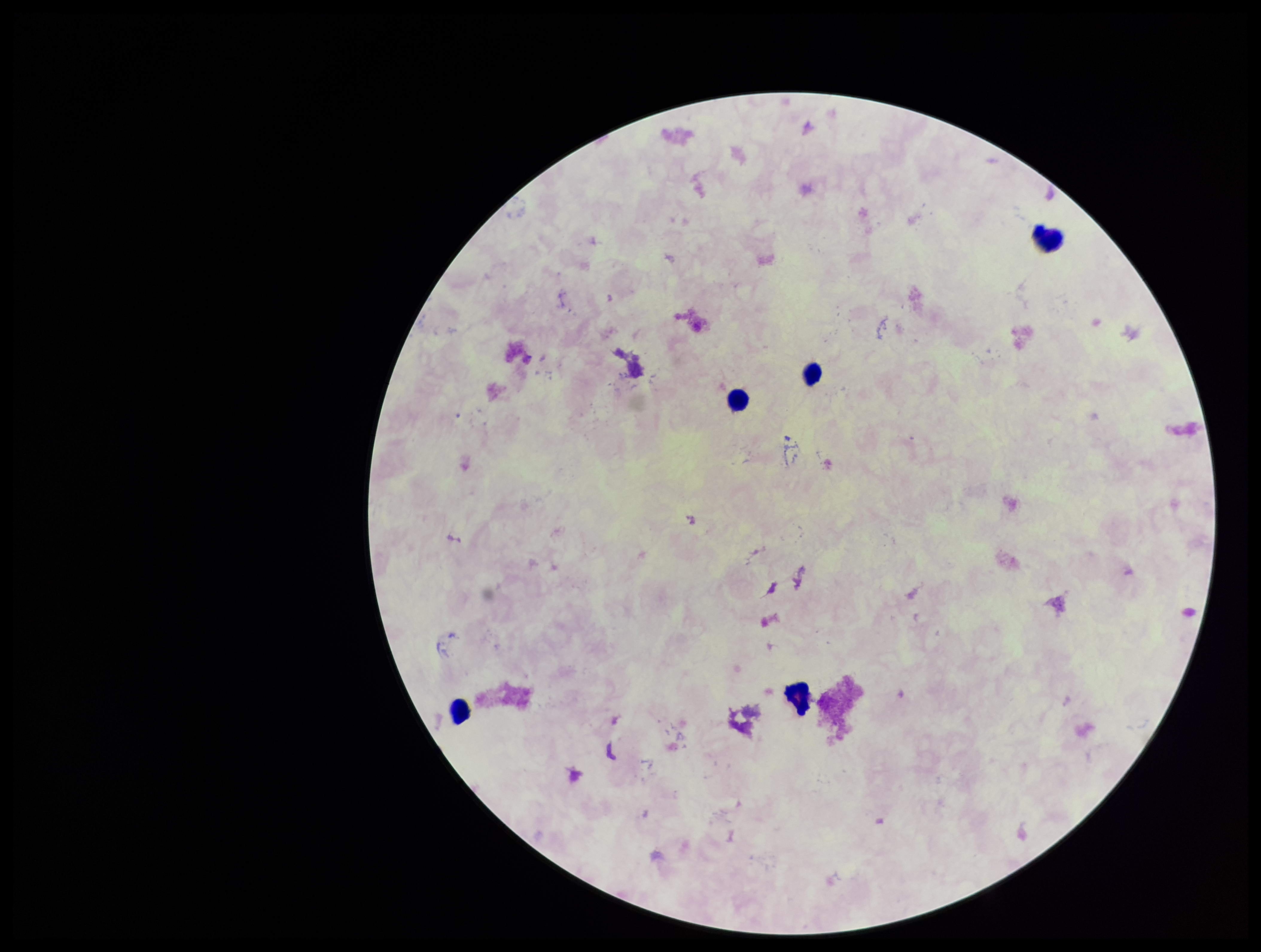

Summary:
  - Plasmodium parasites: none identified
  - Stain: Giemsa
  - Capture: smartphone photograph through the microscope eyepiece
  - Patient malaria status: negative
  - Parasite count: 0
  - Preparation: thick smear
  - Leukocyte count: 5
  - Field of view: one from this slide
  - Image size: 1261×952 pixels